Give the position of every malaria parasite.
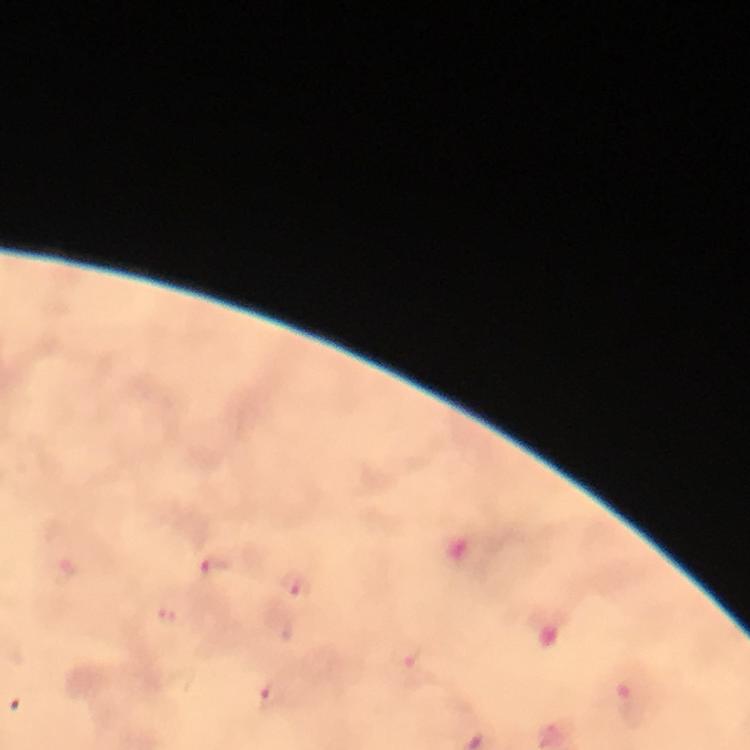

Approximate object centers, in pixels from the top-left corner.
Malaria parasites: (x=214, y=568), (x=295, y=591), (x=169, y=616), (x=409, y=658), (x=272, y=695).

Summary:
  - Preparation: thick blood smear
  - Magnification: 100x
  - Stain: Giemsa
  - Image size: 750×750 pixels
  - Cropped from: a single field of view
  - Context: from a malaria diagnostic workup
  - Immersion oil: used
  - Capture: smartphone camera through the microscope